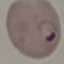 Result: malaria parasites detected. Acquired by smartphone through the microscope eyepiece. Thin blood film. Giemsa stain. Automatically extracted cell patch, resized to 64 × 64 pixels.